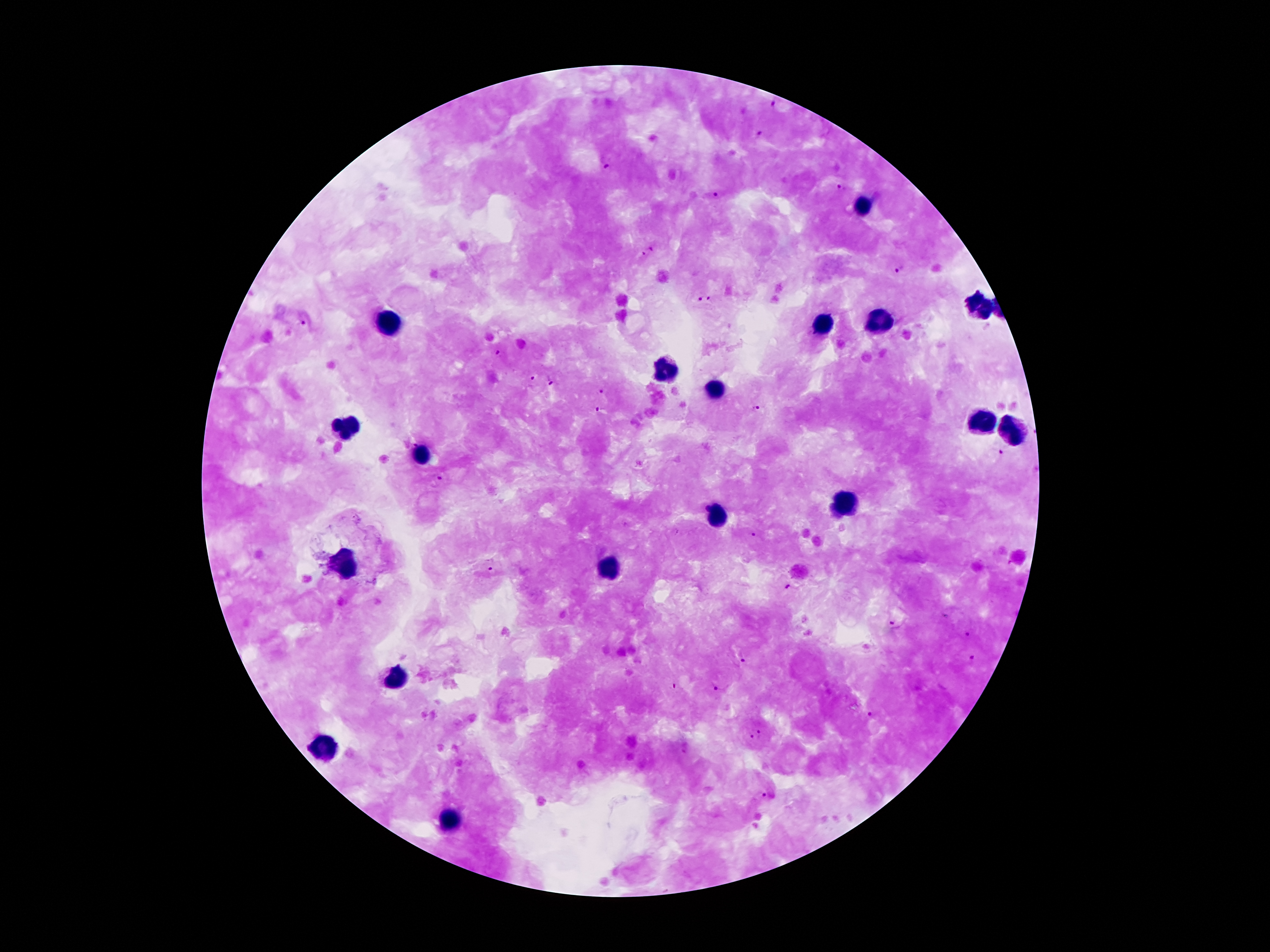 Approximate centers as {x, y} in pixels. Leukocyte locations: {865, 203}, {978, 306}, {388, 319}, {878, 323}, {821, 325}, {666, 369}, {714, 388}, {978, 420}, {346, 428}, {1014, 430}, {422, 451}, {850, 506}, {720, 513}, {348, 561}, {609, 564}, {395, 677}, {325, 749}, {449, 819}. Plasmodium parasite locations: {774, 101}, {761, 136}, {606, 167}, {843, 188}, {714, 195}, {649, 249}, {899, 271}, {704, 300}, {304, 322}, {498, 353}, {531, 376}, {551, 383}, {602, 390}, {600, 409}, {756, 409}, {997, 453}, {442, 478}, {755, 535}, {489, 567}, {790, 587}, {946, 615}, {892, 626}, {967, 633}, {971, 657}, {742, 663}, {673, 684}, {717, 687}, {872, 714}, {756, 735}, {768, 795}. 100x magnification. Thick blood smear. Photographed through the microscope eyepiece with a smartphone camera. Single field of view. Giemsa stain. Image is 1270×952 pixels. Patient malaria status: positive for Plasmodium falciparum.